Classify this cell by malaria status.
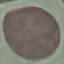

It is uninfected.

Summary:
  - Image type: cell patch, automatically extracted from a larger field of view and resized to 64 × 64 pixels
  - Capture: smartphone camera at the microscope eyepiece
  - Preparation: thin smear
  - Stain: Giemsa